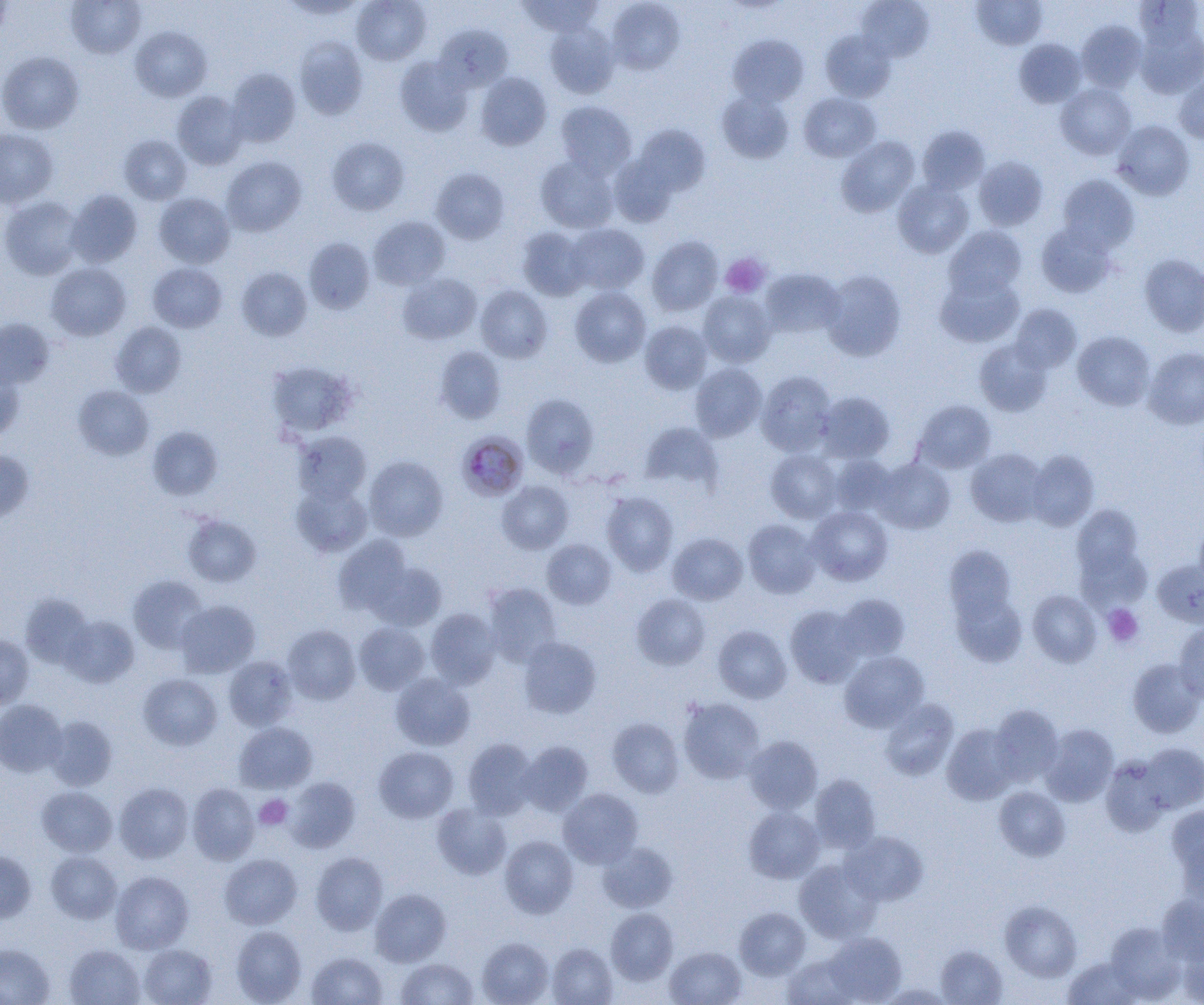
Summary:
  - Coordinate format: approximate bounding boxes as named x1/y1/x2/y2 corners in pixels
  - Plasmodium malariae-infected red blood cell locations: (x1=458, y1=432, x2=528, y2=501)
  - Uninfected red blood cell locations: (x1=66, y1=0, x2=145, y2=59), (x1=280, y1=0, x2=366, y2=20), (x1=351, y1=0, x2=431, y2=65), (x1=519, y1=0, x2=603, y2=38), (x1=607, y1=0, x2=685, y2=74), (x1=971, y1=0, x2=1047, y2=49), (x1=1135, y1=0, x2=1203, y2=52), (x1=0, y1=1, x2=12, y2=41), (x1=856, y1=1, x2=934, y2=61), (x1=1076, y1=21, x2=1147, y2=92), (x1=544, y1=23, x2=619, y2=99), (x1=435, y1=25, x2=513, y2=91), (x1=131, y1=26, x2=212, y2=101), (x1=1135, y1=26, x2=1204, y2=99), (x1=820, y1=30, x2=896, y2=102), (x1=727, y1=33, x2=809, y2=108), (x1=294, y1=36, x2=368, y2=120), (x1=1014, y1=38, x2=1086, y2=107), (x1=0, y1=51, x2=84, y2=134), (x1=395, y1=56, x2=474, y2=136), (x1=226, y1=68, x2=301, y2=147), (x1=475, y1=72, x2=552, y2=150), (x1=1174, y1=75, x2=1204, y2=143), (x1=1056, y1=83, x2=1136, y2=159), (x1=717, y1=90, x2=794, y2=163), (x1=172, y1=91, x2=248, y2=169), (x1=799, y1=92, x2=881, y2=162), (x1=555, y1=101, x2=637, y2=178), (x1=1113, y1=120, x2=1195, y2=200), (x1=631, y1=124, x2=711, y2=199), (x1=917, y1=125, x2=990, y2=194), (x1=0, y1=129, x2=58, y2=208), (x1=119, y1=135, x2=192, y2=205), (x1=327, y1=136, x2=410, y2=215), (x1=836, y1=136, x2=920, y2=216), (x1=535, y1=155, x2=619, y2=234), (x1=221, y1=156, x2=306, y2=236), (x1=974, y1=156, x2=1048, y2=231), (x1=431, y1=168, x2=509, y2=244), (x1=1058, y1=174, x2=1139, y2=252), (x1=893, y1=180, x2=973, y2=258), (x1=66, y1=189, x2=143, y2=268), (x1=154, y1=193, x2=234, y2=268), (x1=0, y1=195, x2=84, y2=280), (x1=369, y1=216, x2=449, y2=290), (x1=1036, y1=222, x2=1117, y2=298), (x1=566, y1=223, x2=649, y2=295), (x1=945, y1=226, x2=1027, y2=298), (x1=517, y1=227, x2=591, y2=300), (x1=646, y1=236, x2=723, y2=316), (x1=303, y1=237, x2=375, y2=314), (x1=1139, y1=254, x2=1204, y2=337), (x1=46, y1=262, x2=131, y2=340), (x1=147, y1=262, x2=227, y2=332), (x1=236, y1=267, x2=312, y2=340), (x1=760, y1=268, x2=845, y2=338), (x1=822, y1=270, x2=906, y2=360), (x1=935, y1=271, x2=1024, y2=347), (x1=397, y1=272, x2=482, y2=344), (x1=476, y1=286, x2=553, y2=363), (x1=570, y1=287, x2=651, y2=367), (x1=698, y1=291, x2=776, y2=367), (x1=1010, y1=304, x2=1082, y2=373), (x1=0, y1=318, x2=54, y2=390), (x1=640, y1=320, x2=712, y2=394), (x1=110, y1=321, x2=186, y2=397), (x1=1073, y1=331, x2=1155, y2=410), (x1=974, y1=339, x2=1053, y2=416), (x1=435, y1=346, x2=506, y2=424), (x1=1143, y1=346, x2=1204, y2=429), (x1=266, y1=360, x2=360, y2=438), (x1=690, y1=363, x2=767, y2=441), (x1=0, y1=370, x2=24, y2=443), (x1=756, y1=370, x2=836, y2=455), (x1=73, y1=385, x2=154, y2=460), (x1=818, y1=391, x2=895, y2=463), (x1=522, y1=393, x2=599, y2=478), (x1=914, y1=400, x2=996, y2=473), (x1=640, y1=422, x2=723, y2=492), (x1=147, y1=426, x2=223, y2=500), (x1=293, y1=431, x2=371, y2=504), (x1=966, y1=448, x2=1047, y2=526), (x1=766, y1=449, x2=842, y2=522), (x1=0, y1=450, x2=34, y2=524), (x1=1026, y1=450, x2=1099, y2=531), (x1=829, y1=455, x2=897, y2=517), (x1=364, y1=456, x2=448, y2=541), (x1=873, y1=458, x2=955, y2=533), (x1=497, y1=480, x2=573, y2=554), (x1=292, y1=483, x2=372, y2=557), (x1=602, y1=491, x2=678, y2=575), (x1=1071, y1=504, x2=1144, y2=581), (x1=807, y1=505, x2=893, y2=585), (x1=182, y1=514, x2=261, y2=587), (x1=743, y1=518, x2=821, y2=598), (x1=1194, y1=520, x2=1204, y2=592), (x1=668, y1=532, x2=748, y2=604), (x1=333, y1=534, x2=414, y2=614), (x1=1074, y1=534, x2=1152, y2=614), (x1=542, y1=539, x2=616, y2=609), (x1=943, y1=544, x2=1019, y2=634), (x1=1153, y1=560, x2=1204, y2=627), (x1=368, y1=561, x2=447, y2=631), (x1=128, y1=575, x2=208, y2=653), (x1=483, y1=583, x2=562, y2=665), (x1=950, y1=588, x2=1027, y2=667), (x1=1028, y1=589, x2=1101, y2=667), (x1=631, y1=593, x2=710, y2=670), (x1=835, y1=593, x2=909, y2=662), (x1=20, y1=594, x2=94, y2=668), (x1=176, y1=600, x2=260, y2=677), (x1=785, y1=605, x2=863, y2=687), (x1=425, y1=608, x2=502, y2=688), (x1=60, y1=615, x2=139, y2=687), (x1=354, y1=622, x2=430, y2=695), (x1=1174, y1=622, x2=1204, y2=703), (x1=282, y1=624, x2=361, y2=704), (x1=713, y1=625, x2=791, y2=702), (x1=0, y1=635, x2=34, y2=707), (x1=518, y1=636, x2=601, y2=718), (x1=840, y1=651, x2=929, y2=732), (x1=224, y1=656, x2=298, y2=730), (x1=1127, y1=658, x2=1203, y2=738), (x1=390, y1=673, x2=475, y2=751), (x1=138, y1=674, x2=222, y2=750), (x1=679, y1=697, x2=764, y2=783), (x1=0, y1=699, x2=67, y2=777), (x1=880, y1=699, x2=959, y2=780), (x1=989, y1=704, x2=1064, y2=785), (x1=44, y1=715, x2=117, y2=790), (x1=607, y1=718, x2=684, y2=798), (x1=234, y1=722, x2=318, y2=793), (x1=942, y1=723, x2=1019, y2=804), (x1=1040, y1=724, x2=1119, y2=806), (x1=743, y1=735, x2=823, y2=814), (x1=462, y1=738, x2=538, y2=818), (x1=518, y1=741, x2=593, y2=816), (x1=1139, y1=743, x2=1204, y2=813), (x1=374, y1=746, x2=458, y2=822), (x1=1100, y1=755, x2=1173, y2=837), (x1=809, y1=774, x2=880, y2=852), (x1=284, y1=777, x2=360, y2=852), (x1=114, y1=783, x2=193, y2=863), (x1=187, y1=783, x2=260, y2=864), (x1=37, y1=786, x2=117, y2=857), (x1=994, y1=786, x2=1070, y2=860), (x1=558, y1=788, x2=643, y2=868), (x1=432, y1=803, x2=511, y2=879), (x1=1167, y1=804, x2=1204, y2=890), (x1=744, y1=806, x2=823, y2=882), (x1=841, y1=830, x2=929, y2=906), (x1=499, y1=835, x2=578, y2=918), (x1=598, y1=841, x2=677, y2=913), (x1=0, y1=851, x2=36, y2=923), (x1=46, y1=851, x2=121, y2=923), (x1=311, y1=852, x2=387, y2=935), (x1=219, y1=854, x2=302, y2=929), (x1=794, y1=858, x2=881, y2=943), (x1=111, y1=871, x2=193, y2=954), (x1=371, y1=889, x2=451, y2=966), (x1=1156, y1=896, x2=1204, y2=966), (x1=1000, y1=901, x2=1082, y2=981), (x1=734, y1=907, x2=810, y2=979), (x1=606, y1=908, x2=678, y2=985), (x1=1105, y1=923, x2=1183, y2=1000), (x1=231, y1=926, x2=306, y2=1004), (x1=823, y1=932, x2=906, y2=1004), (x1=477, y1=937, x2=555, y2=1005), (x1=1179, y1=941, x2=1204, y2=1005), (x1=0, y1=943, x2=54, y2=1005), (x1=547, y1=943, x2=617, y2=1005), (x1=139, y1=944, x2=216, y2=1005), (x1=64, y1=945, x2=145, y2=1005), (x1=936, y1=945, x2=1007, y2=1004), (x1=665, y1=946, x2=746, y2=1005), (x1=306, y1=952, x2=387, y2=1005), (x1=783, y1=954, x2=859, y2=1005), (x1=1063, y1=957, x2=1142, y2=1004), (x1=395, y1=958, x2=478, y2=1004)
  - Platelet locations: (x1=720, y1=253, x2=770, y2=298), (x1=1103, y1=604, x2=1143, y2=647), (x1=255, y1=794, x2=293, y2=830)
  - Slide-level diagnosis: Plasmodium malariae
  - Preparation: thin blood film
  - Modality: optical microscopy
  - Magnification: 1000x
  - Image size: 1204×1005 pixels
  - Field of view: single